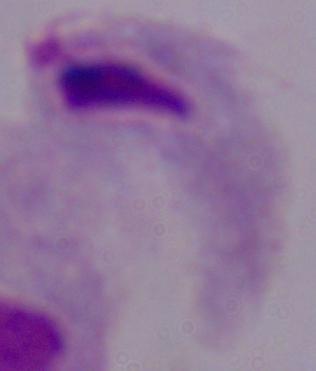 Captured at 1000x magnification. A trichomonad is seen. Micrograph.